Assess this cell for malaria.
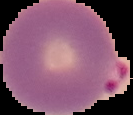

It is parasitized.

Cell region segmented out of the field of view; the surrounding area is masked to black. Image is 133×115 pixels. From a thin blood smear.